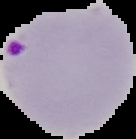
Result: malaria parasites detected. From a thin blood smear. Segmented cell region on a black background. Image is 136×139 pixels.